Identify the parasite.
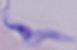

A trypanosome.

Captured at 1000x magnification. Micrograph.